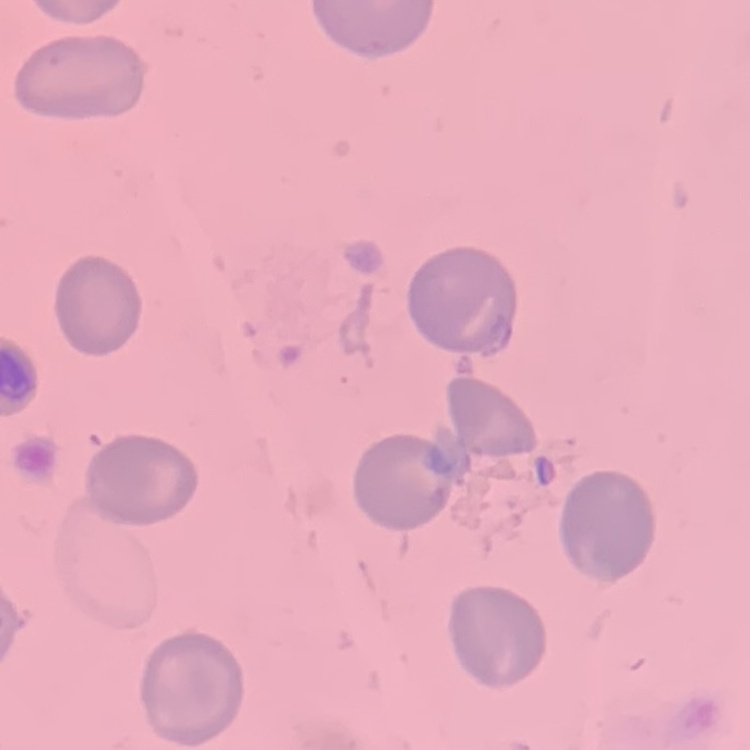

Summary:
  - Red blood cell morphology: no rouleaux formation
  - Preparation: thin peripheral smear
  - Image type: one tile cut from a larger photomicrograph
  - Stain: Field's or Giemsa